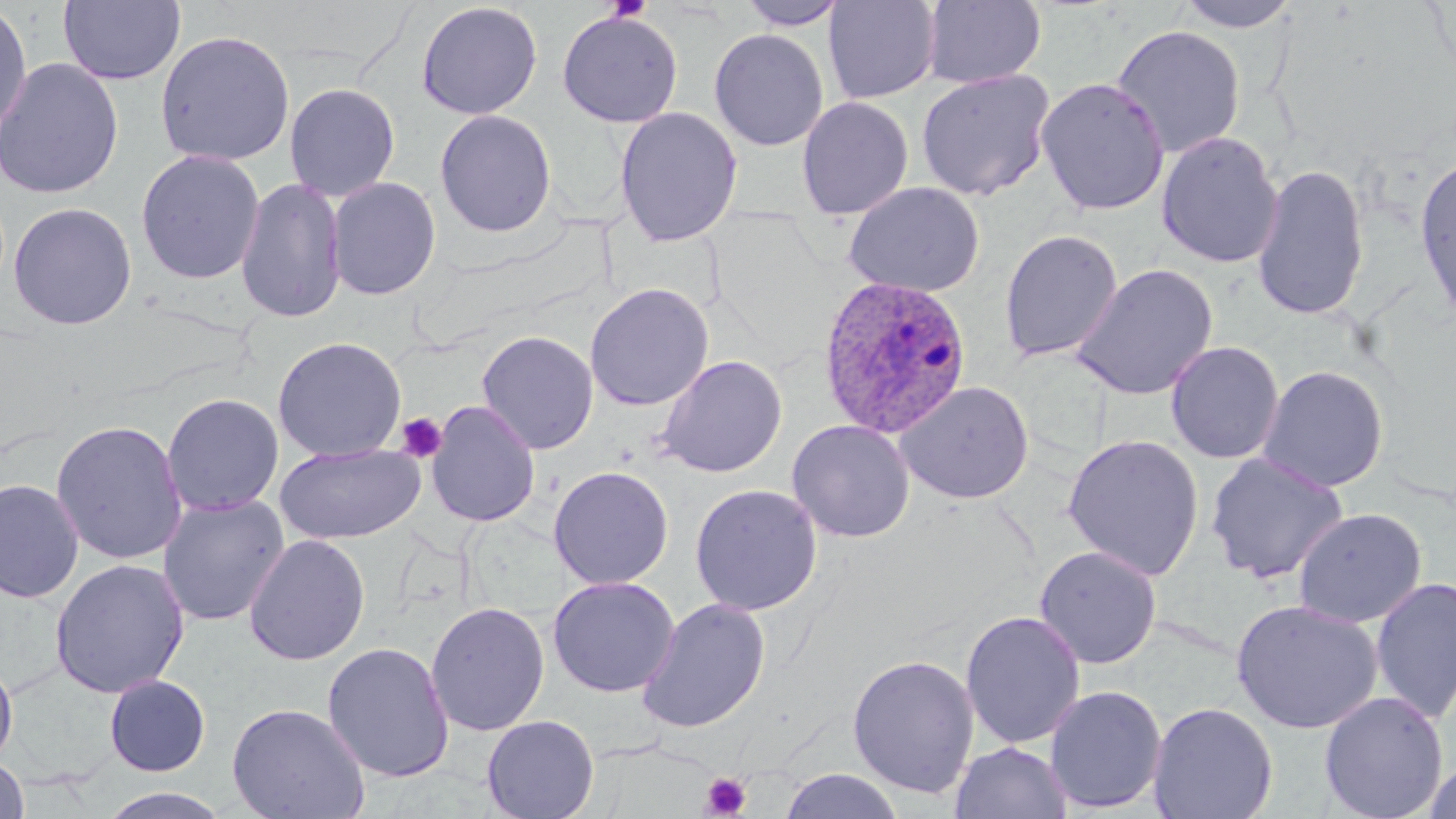
Summary:
  - Coordinate format: approximate bounding boxes as (x1,y1)-(x2,y2) corner pairs in pixels
  - Uninfected red blood cell locations: (57,0)-(187,86), (736,0)-(849,30), (923,0)-(1046,88), (1173,0)-(1301,33), (0,1)-(33,145), (415,1)-(543,120), (823,1)-(941,104), (556,9)-(684,128), (1110,24)-(1247,159), (709,28)-(829,151), (154,29)-(295,167), (0,57)-(124,200), (916,68)-(1055,201), (1035,77)-(1170,216), (284,82)-(400,202), (797,95)-(914,219), (614,106)-(743,247), (434,109)-(557,238), (1156,131)-(1283,269), (135,148)-(265,285), (1414,151)-(1456,327), (1251,163)-(1370,322), (236,176)-(347,324), (326,176)-(441,301), (843,181)-(984,298), (8,202)-(138,330), (999,228)-(1123,362), (1070,263)-(1218,401), (585,282)-(714,411), (477,330)-(599,454), (272,336)-(407,463), (1165,341)-(1284,464), (655,354)-(788,478), (1257,365)-(1389,493), (895,380)-(1034,504), (161,392)-(284,516), (426,401)-(541,527), (50,419)-(188,565), (786,419)-(915,542), (1061,433)-(1204,581), (275,443)-(425,544), (1205,451)-(1348,584), (548,465)-(674,590), (0,478)-(84,604), (689,483)-(823,616), (157,495)-(290,626), (1292,507)-(1427,628), (244,534)-(371,666), (1034,545)-(1162,669), (50,559)-(190,699), (547,576)-(680,697), (1369,576)-(1456,724), (636,598)-(771,734), (1230,599)-(1385,735), (426,601)-(550,737), (959,610)-(1086,749), (321,641)-(455,783), (846,653)-(980,798), (0,656)-(18,770), (104,674)-(211,777), (1044,684)-(1167,814), (1319,691)-(1448,819), (1148,701)-(1279,819), (226,702)-(370,819), (482,715)-(599,819), (950,741)-(1073,819), (0,755)-(30,818), (1422,758)-(1456,819), (778,768)-(905,819), (99,786)-(231,819)
  - Platelet locations: (395,412)-(448,464), (701,772)-(752,818)
  - Plasmodium ovale-infected red blood cell locations: (817,274)-(972,438)
  - Slide-level diagnosis: Plasmodium ovale
  - Modality: optical microscopy
  - Magnification: 1000x
  - Image size: 1456×819 pixels
  - Stain: May-Grünwald-Giemsa
  - Preparation: thin blood smear
  - Field of view: one of a larger specimen